State which parasite is depicted.
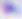

This is Toxoplasma gondii.

400x magnification. Micrograph.